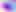
modality = micrograph
identification = Toxoplasma gondii
magnification = 400x